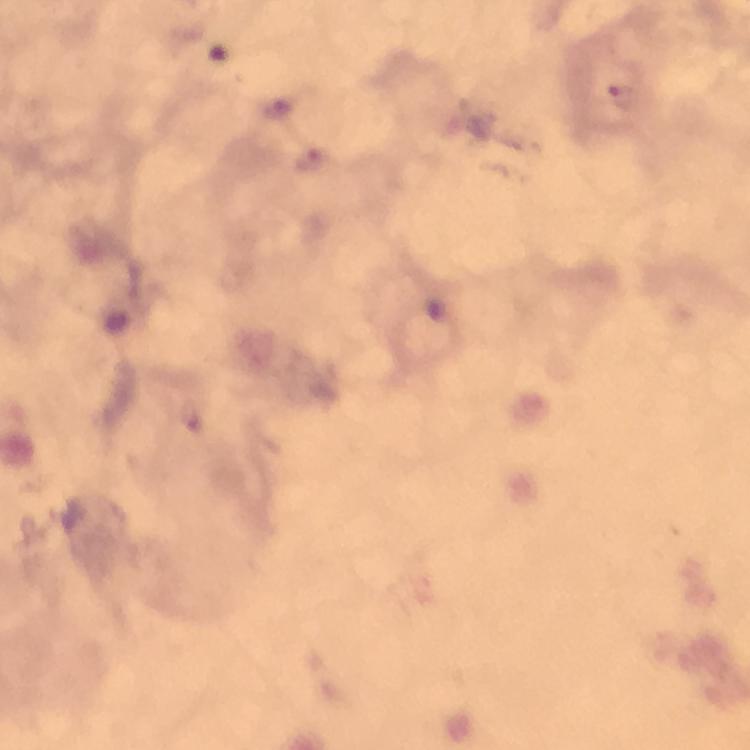
magnification: 100x
stain: Giemsa
plasmodium_parasite_locations: 'approximate object centers, in pixels from the top-left corner: (x=619, y=95), (x=280, y=107), (x=310, y=159)'
image_size: 750×750 pixels
preparation: thick blood film
immersion_oil: used
capture: smartphone photograph through a microscope
context: from a diagnostic examination for malaria
cropped_from: one field of view